Locate every blood parasite and identify its species.
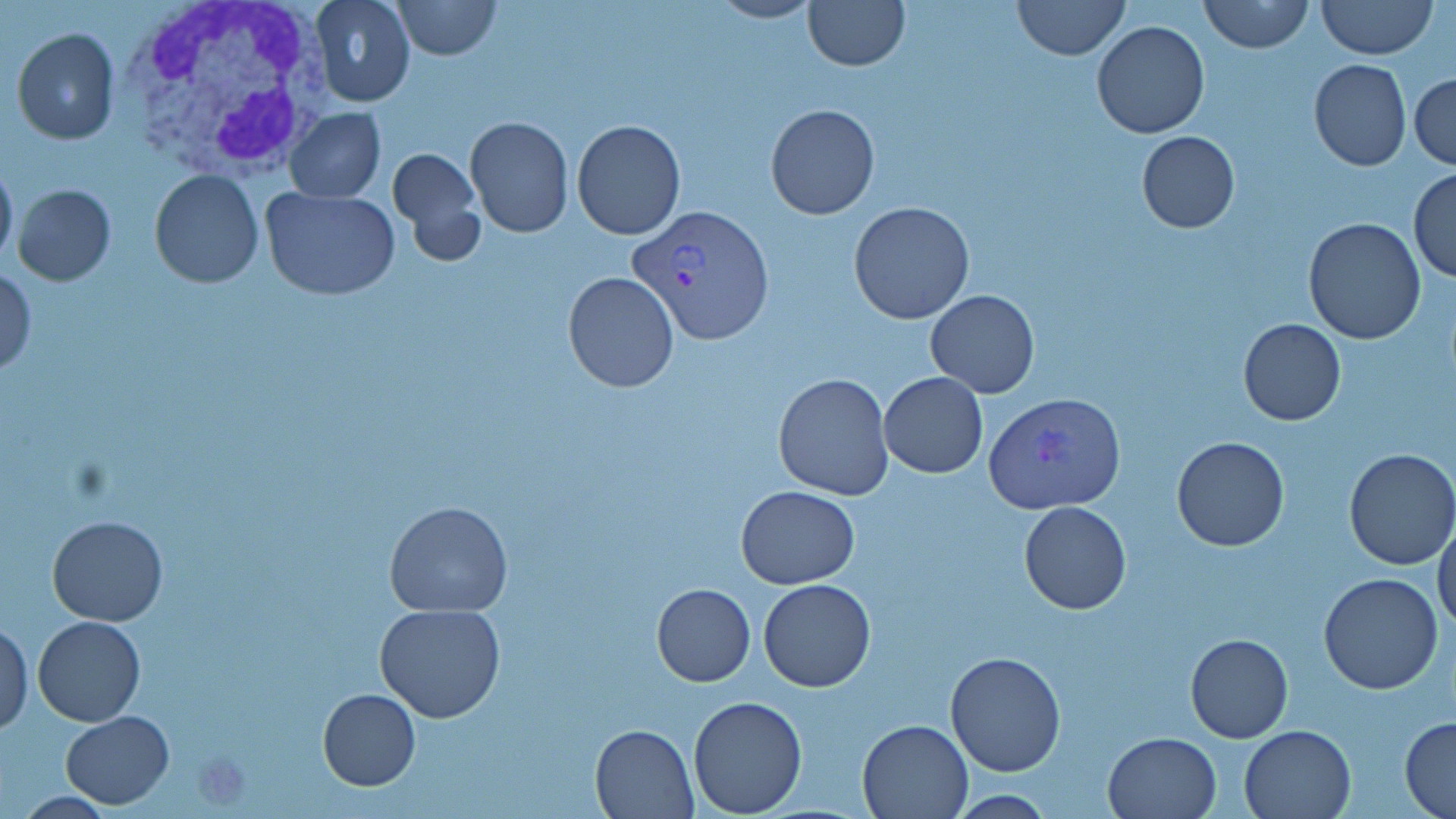

Approximate bounding boxes as named x1/y1/x2/y2 corners in pixels.
Plasmodium vivax-infected red blood cells: (x1=626, y1=203, x2=776, y2=346), (x1=985, y1=391, x2=1126, y2=515).
No Plasmodium falciparum, Plasmodium ovale, Plasmodium malariae, Babesia divergens, or Trypanosoma brucei observed.

Uninfected red blood cell locations: (x1=310, y1=0, x2=414, y2=108), (x1=391, y1=0, x2=501, y2=60), (x1=707, y1=0, x2=822, y2=24), (x1=803, y1=0, x2=910, y2=70), (x1=1013, y1=0, x2=1127, y2=60), (x1=1198, y1=0, x2=1314, y2=53), (x1=1317, y1=0, x2=1436, y2=60), (x1=1091, y1=20, x2=1211, y2=139), (x1=12, y1=28, x2=121, y2=146), (x1=1308, y1=58, x2=1410, y2=171), (x1=1408, y1=72, x2=1456, y2=170), (x1=765, y1=103, x2=880, y2=220), (x1=285, y1=108, x2=386, y2=203), (x1=463, y1=117, x2=573, y2=237), (x1=571, y1=119, x2=685, y2=238), (x1=1136, y1=130, x2=1239, y2=234), (x1=388, y1=145, x2=487, y2=266), (x1=1, y1=155, x2=18, y2=269), (x1=150, y1=169, x2=264, y2=290), (x1=1408, y1=169, x2=1456, y2=282), (x1=12, y1=183, x2=117, y2=285), (x1=259, y1=184, x2=401, y2=301), (x1=848, y1=200, x2=975, y2=325), (x1=1303, y1=217, x2=1426, y2=345), (x1=0, y1=267, x2=36, y2=378), (x1=563, y1=272, x2=680, y2=393), (x1=926, y1=290, x2=1039, y2=397), (x1=1238, y1=319, x2=1346, y2=425), (x1=773, y1=372, x2=895, y2=501), (x1=878, y1=372, x2=988, y2=478), (x1=1171, y1=436, x2=1290, y2=552), (x1=1342, y1=448, x2=1456, y2=571), (x1=735, y1=485, x2=860, y2=588), (x1=384, y1=500, x2=514, y2=617), (x1=1019, y1=501, x2=1132, y2=613), (x1=45, y1=515, x2=168, y2=626), (x1=1433, y1=516, x2=1456, y2=633), (x1=1318, y1=572, x2=1444, y2=695), (x1=758, y1=578, x2=877, y2=692), (x1=652, y1=582, x2=755, y2=686), (x1=373, y1=603, x2=506, y2=724), (x1=32, y1=615, x2=147, y2=726), (x1=0, y1=620, x2=33, y2=734), (x1=1186, y1=633, x2=1293, y2=742), (x1=945, y1=650, x2=1068, y2=777), (x1=318, y1=688, x2=420, y2=791), (x1=687, y1=695, x2=807, y2=818), (x1=62, y1=711, x2=174, y2=808), (x1=1401, y1=717, x2=1456, y2=817), (x1=857, y1=718, x2=975, y2=818), (x1=589, y1=722, x2=698, y2=818), (x1=1239, y1=723, x2=1355, y2=818), (x1=1104, y1=731, x2=1220, y2=819). White blood cell locations: (x1=118, y1=0, x2=333, y2=181). Platelet locations: (x1=189, y1=749, x2=253, y2=809). Slide-level diagnosis: Plasmodium vivax. 1000x magnification. Optical microscopy. Thin blood film. Image is 1456×819 pixels. May-Grünwald-Giemsa stain. One field of a larger specimen.